Assess this cell for malaria.
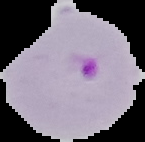
It is parasitized.

From a thin blood film. Image is 145×142 pixels. Cell region segmented out of the field of view; the surrounding area is masked to black.